Outline each blood parasite and name the species.
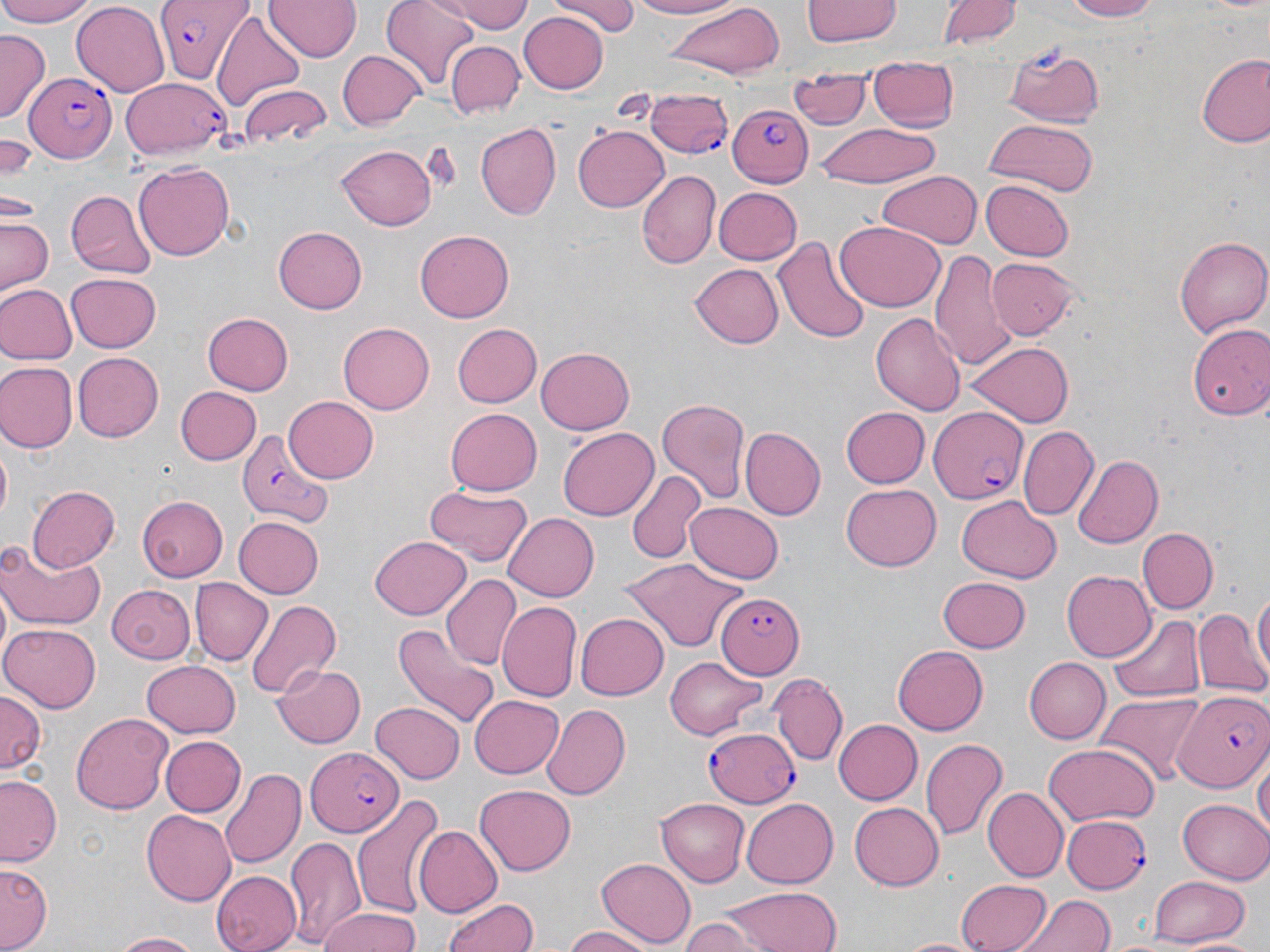
Approximate bounding boxes as (x1,y1)-(x2,y2) corner pairs in pixels.
Plasmodium falciparum-infected red blood cells: (155,0)-(250,82), (22,71)-(117,163), (123,77)-(229,161), (645,89)-(735,157), (727,100)-(813,187), (930,407)-(1030,503), (234,426)-(330,525), (716,593)-(802,678), (1176,692)-(1270,793), (706,726)-(801,805), (303,744)-(407,833), (1060,813)-(1151,894).
No Plasmodium ovale, Plasmodium malariae, Plasmodium vivax, Babesia divergens, or Trypanosoma brucei observed.

Uninfected red blood cell locations: (0,0)-(98,26), (264,0)-(359,61), (380,0)-(483,86), (441,0)-(532,33), (551,0)-(640,34), (626,0)-(739,18), (803,0)-(901,45), (939,0)-(1019,49), (1060,0)-(1160,21), (71,2)-(169,93), (663,4)-(782,78), (519,10)-(609,93), (211,11)-(306,113), (0,31)-(48,120), (445,40)-(524,118), (1002,41)-(1106,126), (337,50)-(425,129), (1195,51)-(1270,146), (867,61)-(958,134), (789,74)-(872,132), (240,84)-(331,148), (981,118)-(1101,196), (474,120)-(561,221), (572,124)-(669,213), (818,124)-(939,186), (0,136)-(40,181), (335,143)-(439,231), (133,161)-(234,261), (636,170)-(719,271), (877,172)-(982,248), (982,179)-(1075,261), (713,186)-(802,265), (66,190)-(156,280), (1,213)-(55,295), (835,220)-(946,311), (273,226)-(368,314), (415,230)-(514,322), (776,236)-(870,343), (1173,237)-(1270,339), (929,251)-(1017,370), (987,257)-(1082,340), (688,263)-(784,349), (65,272)-(163,353), (0,284)-(75,364), (202,312)-(294,394), (869,313)-(966,416), (338,322)-(434,413), (1187,322)-(1270,420), (450,323)-(543,409), (967,340)-(1075,427), (535,346)-(635,435), (72,351)-(163,441), (0,362)-(75,453), (173,385)-(262,465), (283,395)-(379,483), (657,395)-(752,502), (447,407)-(545,496), (841,407)-(930,488), (1019,426)-(1097,521), (557,427)-(658,521), (741,428)-(825,520), (0,445)-(11,528), (1072,453)-(1162,549), (626,471)-(703,563), (26,484)-(120,572), (840,485)-(942,572), (423,487)-(533,566), (958,494)-(1060,580), (136,496)-(230,580), (686,502)-(785,584), (502,510)-(598,600), (232,516)-(322,599), (1138,527)-(1218,612), (369,534)-(471,620), (0,540)-(105,629), (616,559)-(749,653), (1062,571)-(1155,660), (444,573)-(519,668), (935,576)-(1031,653), (190,579)-(270,665), (106,583)-(195,664), (1250,585)-(1269,685), (246,600)-(343,700), (499,604)-(580,701), (1192,606)-(1270,699), (577,611)-(669,699), (1111,614)-(1205,703), (1,622)-(102,711), (393,623)-(500,725), (893,644)-(989,735), (664,656)-(769,739), (1024,656)-(1111,743), (140,660)-(243,738), (274,662)-(366,748), (773,676)-(846,766), (0,689)-(46,776), (1096,691)-(1206,784), (469,694)-(563,778), (370,700)-(466,785), (542,703)-(630,801), (71,713)-(174,813), (834,718)-(922,805), (158,735)-(244,818), (921,739)-(1006,842), (1043,742)-(1156,826), (1254,752)-(1269,845), (220,768)-(304,871), (1,776)-(63,867), (476,786)-(576,875), (982,786)-(1068,882), (350,792)-(443,919), (655,798)-(750,886), (740,798)-(837,888), (1177,798)-(1270,883), (850,803)-(943,889), (139,811)-(238,904), (413,826)-(501,918), (284,836)-(366,949), (596,858)-(694,948), (1,863)-(51,949), (212,869)-(299,952), (1151,874)-(1250,945), (956,876)-(1055,951), (722,884)-(844,952), (442,893)-(539,952), (1018,893)-(1115,952), (315,910)-(425,952), (680,916)-(765,952), (562,925)-(661,952), (110,931)-(204,951), (1102,933)-(1201,952), (1178,934)-(1265,952). Slide-level diagnosis: Plasmodium falciparum. One field of a larger specimen. Thin blood smear. Light microscopy. May-Grünwald-Giemsa stain. Image is 1270×952 pixels. 1000x magnification.